State which parasite is depicted.
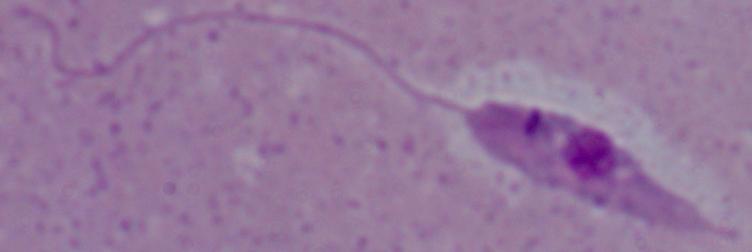

Leishmania.

modality = photomicrograph
magnification = 1000x